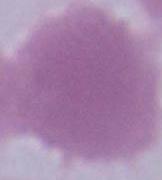
{
  "modality": "micrograph",
  "magnification": "1000x",
  "identification": "erythrocyte"
}